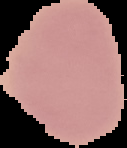
Summary:
  - Image size: 127×148 pixels
  - Preparation: thin blood film
  - Image type: cell region segmented out of the field of view; surrounding area masked to black
  - Malaria status: uninfected